Give the preparation type.
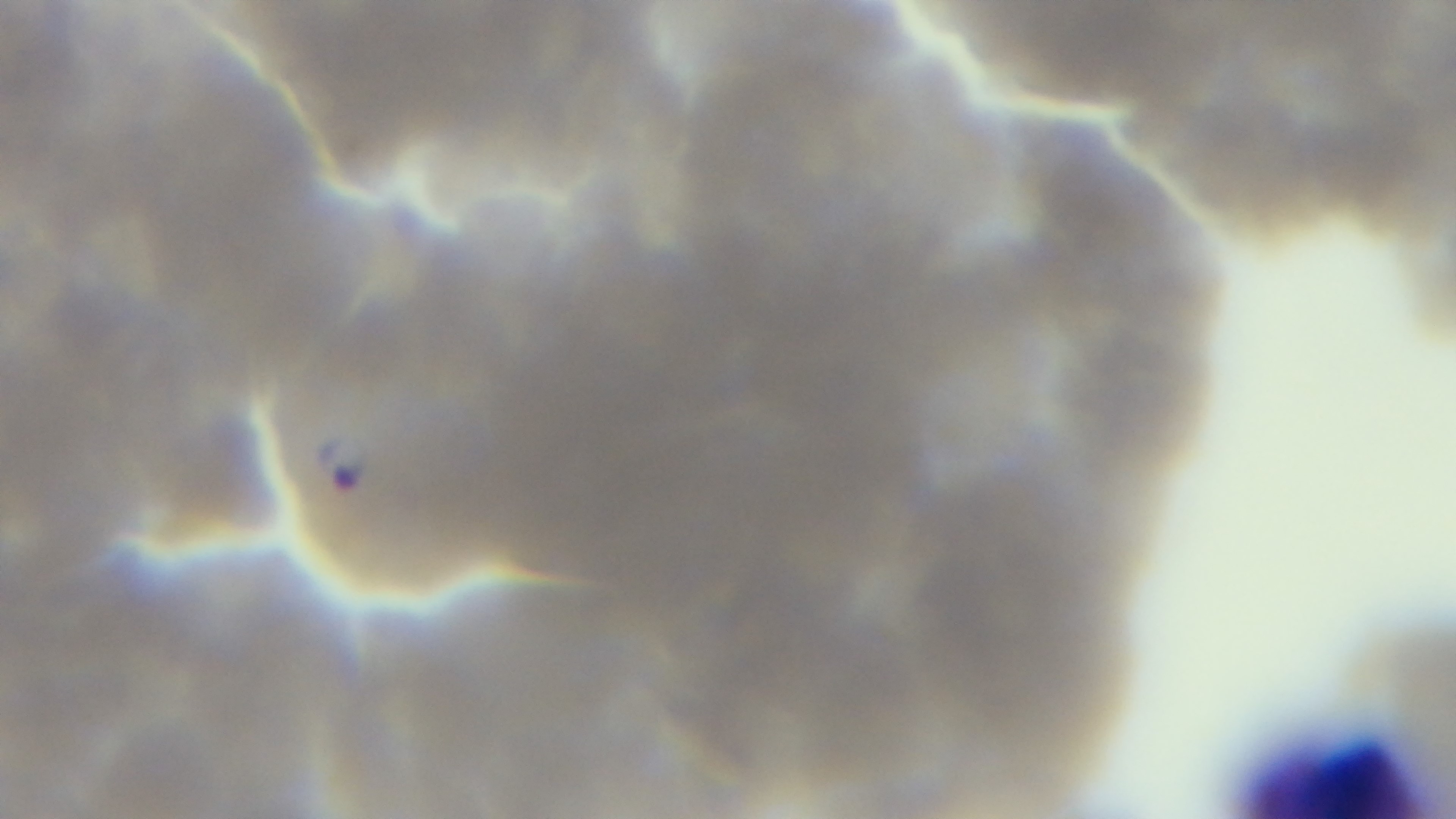

It is a thin blood film.

One field from the slide. Captured with a mounted 4K digital camera. Oil-immersion objective, 100x. Giemsa-stained. Malaria status: infected. Photomicrograph.